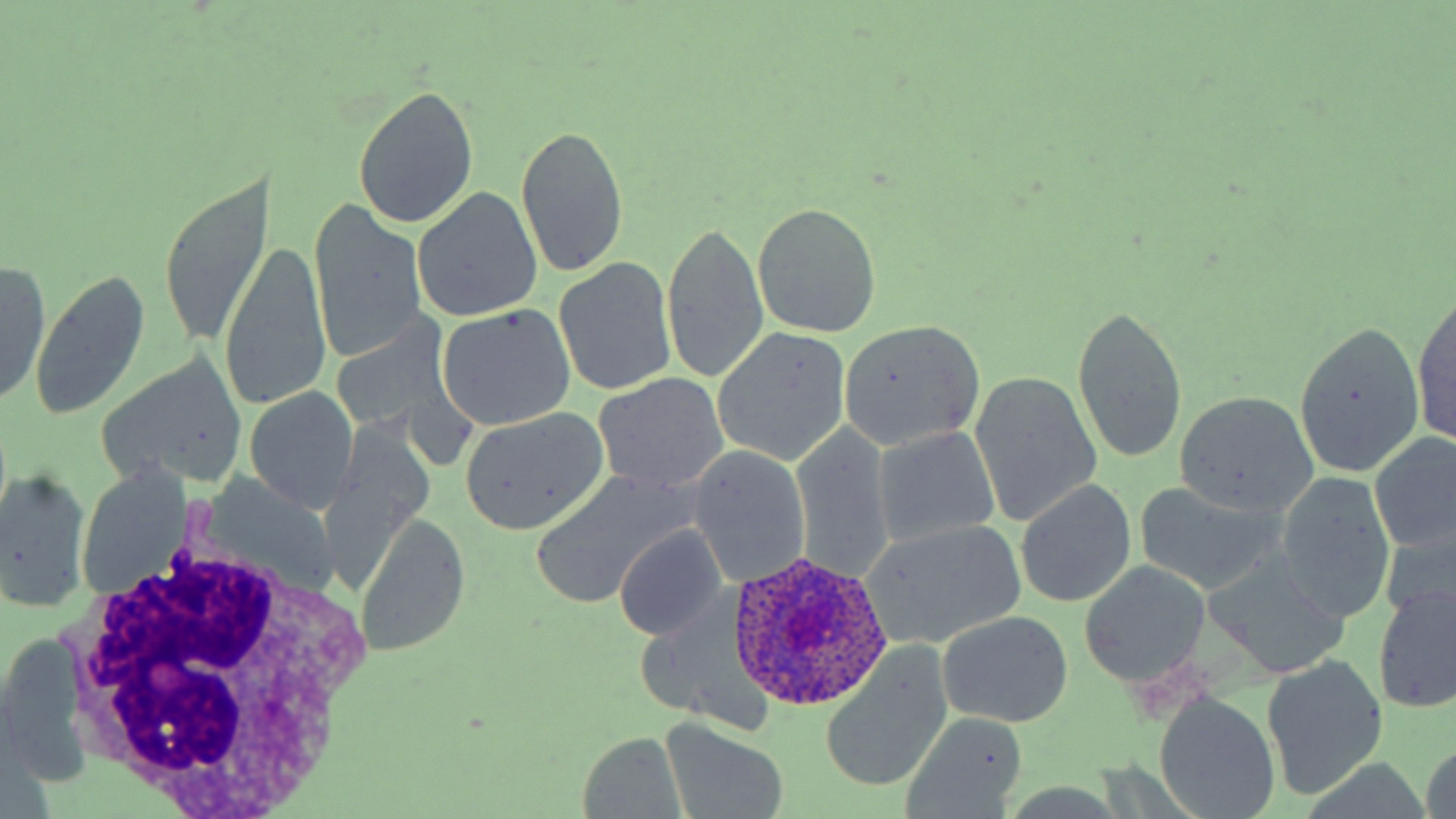

slide-level diagnosis = Plasmodium ovale
magnification = 1000x
modality = optical microscopy
image size = 1456×819 pixels
preparation = thin blood smear
uninfected red blood cell locations = approximate bounding boxes as [x1, y1, x2, y2] in pixels: [353, 83, 479, 230], [516, 126, 629, 276], [157, 176, 272, 344], [415, 189, 541, 323], [308, 200, 428, 369], [752, 202, 881, 336], [662, 221, 769, 386], [219, 241, 331, 416], [556, 255, 678, 398], [0, 260, 51, 410], [31, 270, 151, 419], [1412, 291, 1455, 451], [1070, 301, 1187, 467], [436, 304, 576, 433], [328, 308, 470, 455], [838, 318, 988, 452], [1289, 322, 1427, 479], [711, 327, 850, 467], [98, 350, 251, 492], [970, 370, 1101, 528], [593, 372, 728, 497], [245, 386, 357, 513], [1173, 391, 1317, 519], [456, 408, 609, 536], [791, 422, 896, 585], [874, 426, 1004, 546], [1371, 432, 1455, 554], [688, 446, 812, 587], [1, 469, 92, 614], [530, 472, 695, 612], [1275, 472, 1397, 624], [1015, 478, 1137, 609], [1133, 480, 1282, 596], [354, 512, 469, 660], [860, 519, 1029, 651], [1380, 521, 1455, 630], [615, 526, 727, 641], [1207, 550, 1353, 680], [1080, 562, 1210, 688], [1373, 583, 1455, 715], [938, 612, 1074, 729], [1, 631, 92, 790], [819, 649, 952, 793], [1262, 657, 1390, 800], [1158, 697, 1281, 818], [903, 712, 1030, 815], [660, 718, 790, 819], [577, 732, 689, 817]
stain = May-Grünwald-Giemsa
white blood cell locations = approximate bounding boxes as [x1, y1, x2, y2] in pixels: [57, 533, 382, 811]
Plasmodium ovale-infected red blood cell locations = approximate bounding boxes as [x1, y1, x2, y2] in pixels: [725, 551, 896, 712]
field of view = one of a larger specimen